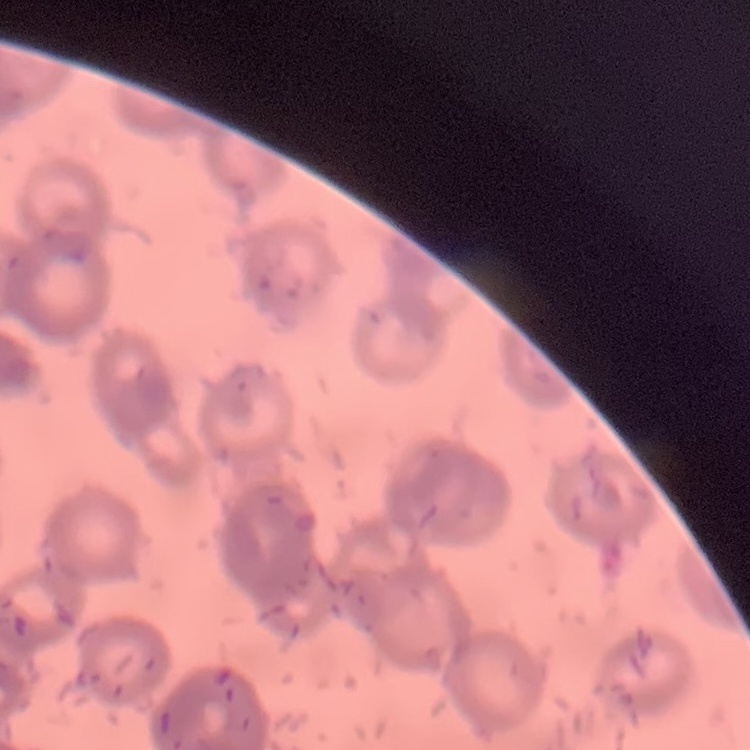

Summary:
  - Red blood cell morphology: rouleaux formation
  - Preparation: thin blood film
  - Image type: one tile cut from a larger photomicrograph
  - Stain: Field's or Giemsa